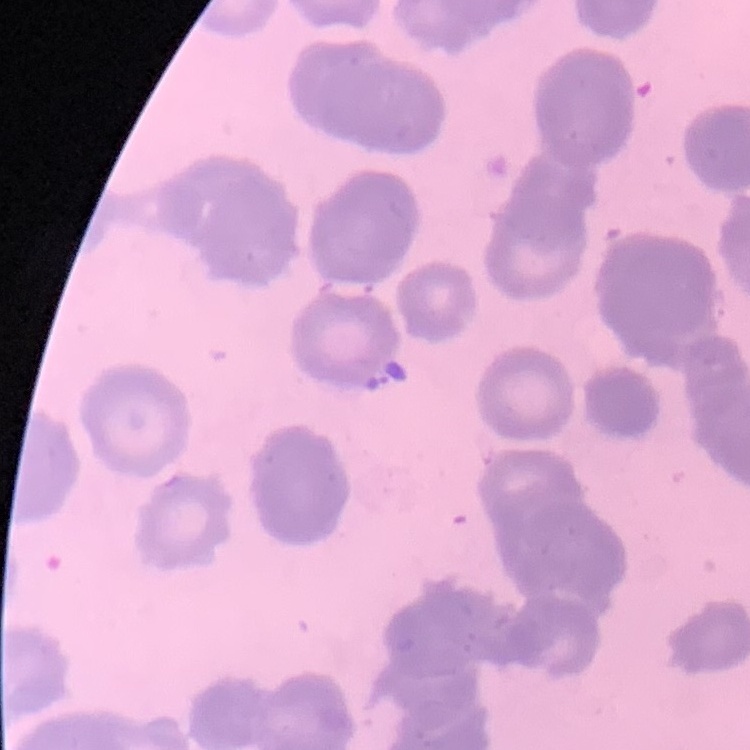
Summary:
  - Erythrocyte morphology: rouleaux formation
  - Preparation: thin peripheral smear
  - Image type: square crop of a larger photomicrograph
  - Stain: Field's or Giemsa